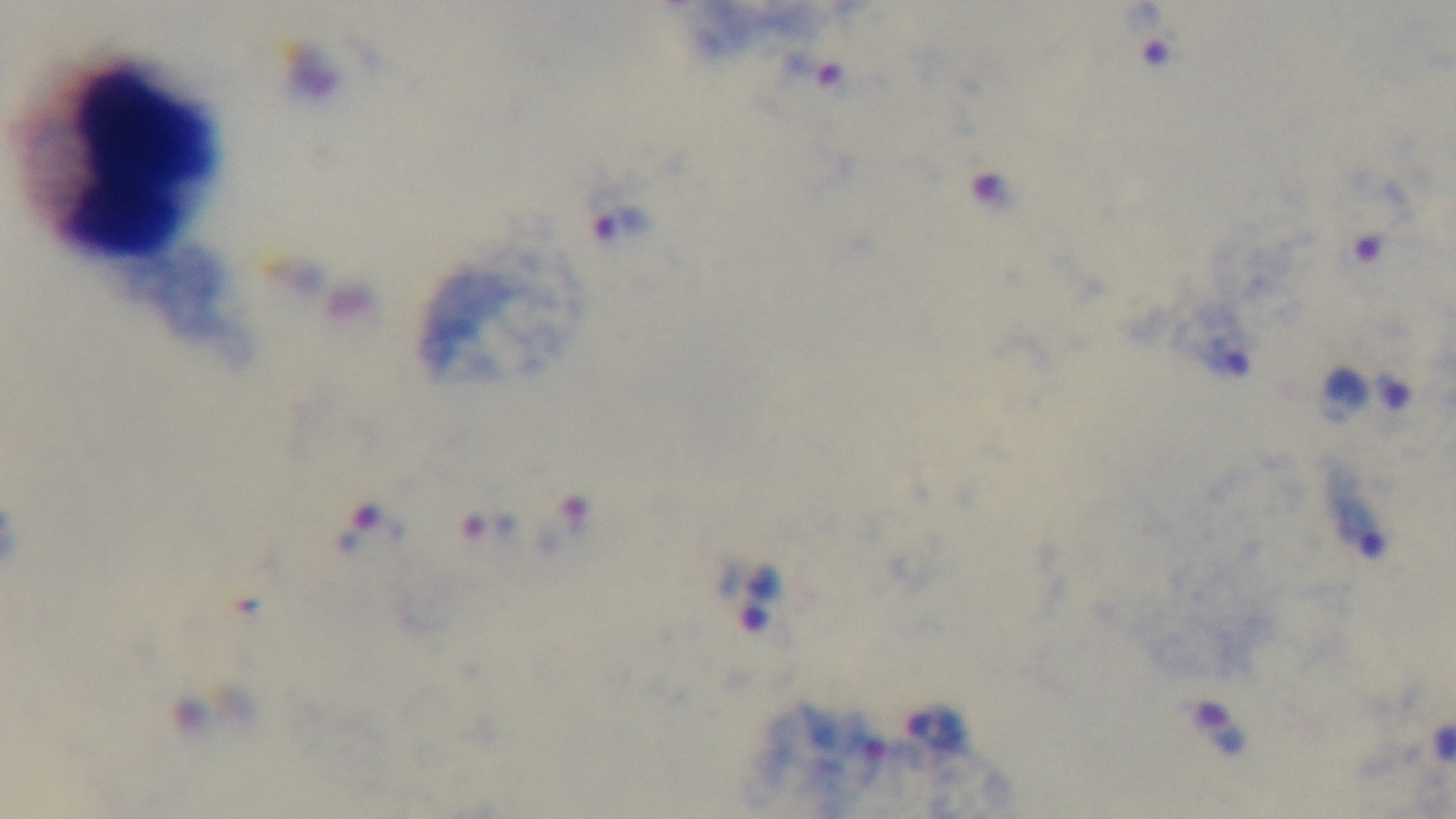
{
  "objective": "100x oil immersion",
  "preparation": "thick smear",
  "field_of_view": "one from the slide",
  "malaria_status": "infected",
  "modality": "light microscopy",
  "stain": "Giemsa",
  "capture": "mounted 4K digital camera"
}